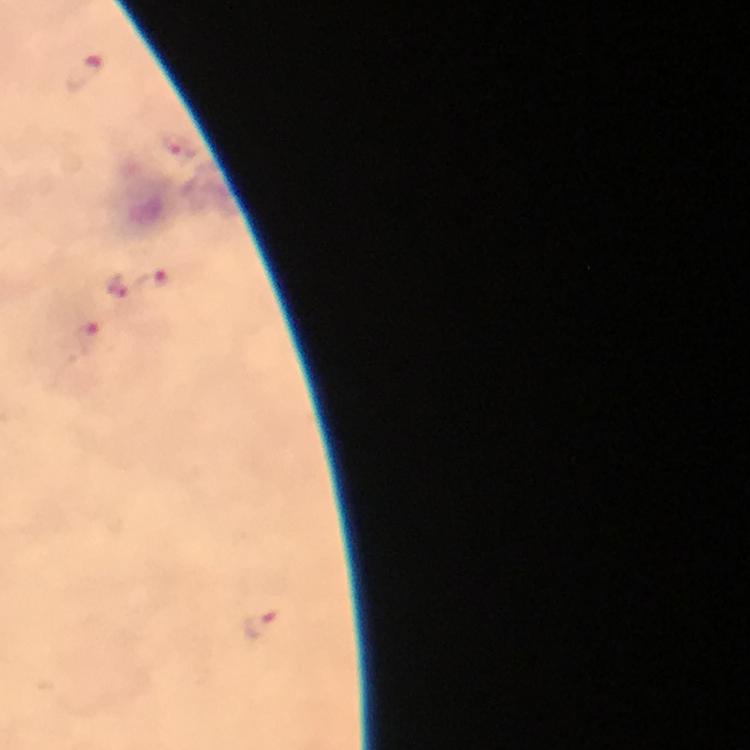
Approximate centers as {x, y} in pixels.
Summary:
  - Plasmodium parasite locations: {85, 74}, {149, 283}, {118, 285}, {86, 340}, {260, 626}
  - Magnification: 100x
  - Stain: Giemsa
  - Cropped from: a single field of view
  - Image size: 750×750 pixels
  - Capture: smartphone photograph through a microscope
  - Immersion oil: applied
  - Context: from a malaria diagnostic workup
  - Preparation: thick smear